Give the position of every malaria parasite.
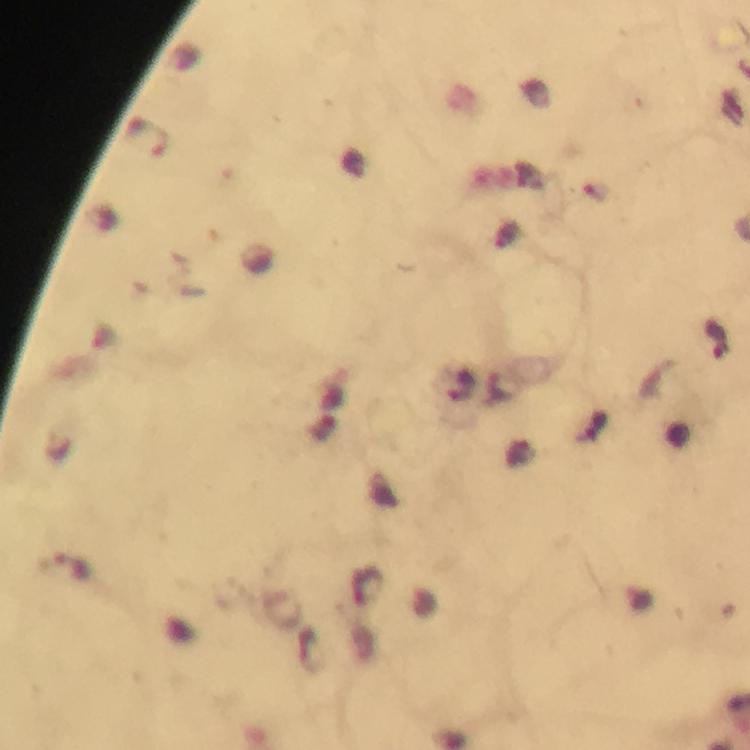

Approximate object centers, in pixels from the top-left corner.
Malaria parasites: (x=148, y=140), (x=65, y=567).

Thick smear. Giemsa-stained preparation. Image is 750×750 pixels. 100x magnification. From a malaria diagnostic workup. Immersion oil applied. Cropped region of a single field of view. Photographed through the microscope with a smartphone camera.